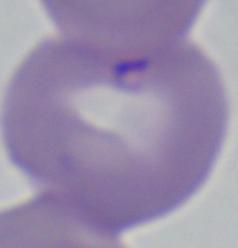
modality = micrograph
magnification = 1000x
identification = Babesia